Identify the parasite.
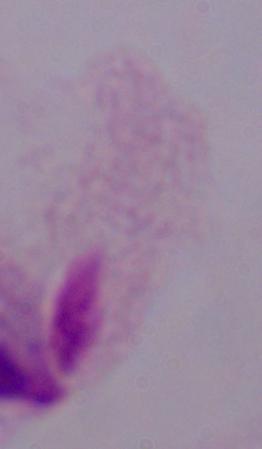
A trichomonad.

Captured at 1000x magnification. Micrograph.